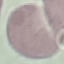

malaria_status: uninfected
stain: Giemsa
image_type: automatically extracted cell patch, resized to 64 × 64 pixels
capture: smartphone through the microscope eyepiece
preparation: thin blood film